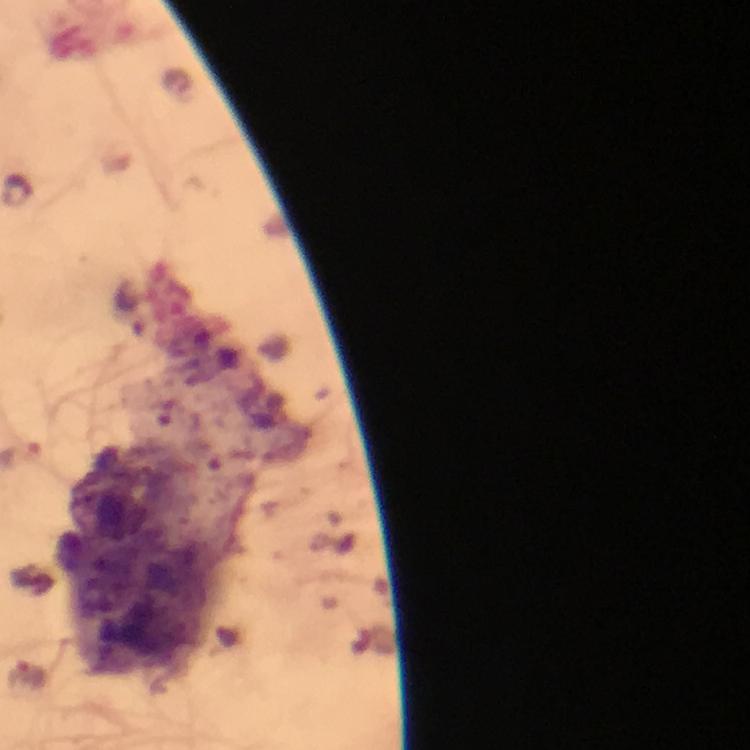
Approximate centers as {x, y} in pixels. Plasmodium parasite locations: {19, 190}. Giemsa-stained preparation. From a diagnostic examination for malaria. Photographed through the microscope with a smartphone camera. Image is 750×750 pixels. Thick blood film. Immersion oil applied. A crop from one field of view. At 100x magnification.